Classify this cell by malaria status.
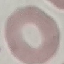
Uninfected.

Summary:
  - Image type: cell patch, automatically extracted from a larger field of view and resized to 64 × 64 pixels
  - Preparation: thin smear
  - Capture: smartphone through the microscope eyepiece
  - Stain: Giemsa